Assess this cell for malaria.
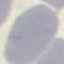
Uninfected.

Summary:
  - Capture: smartphone through the microscope eyepiece
  - Preparation: thin blood film
  - Stain: Giemsa
  - Image type: cell patch, automatically extracted from a larger field of view and resized to 64 × 64 pixels